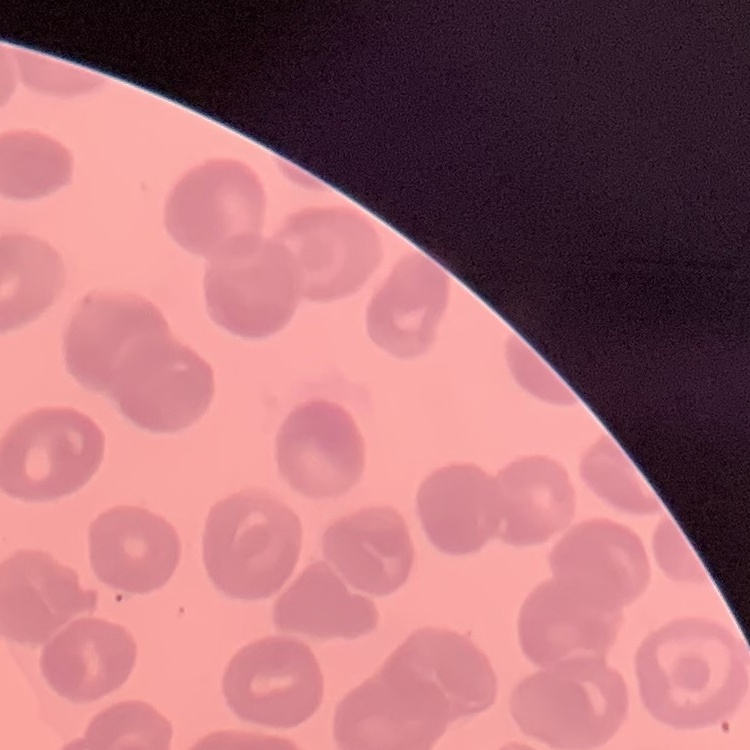
The red blood cells show no rouleaux formation. Stained with either Field's or Giemsa. Thin blood film. Square crop of a larger photomicrograph.